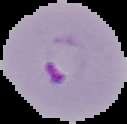
result: malaria parasites identified
image_type: cell region segmented out of the field of view; surrounding area masked to black
image_size: 127×124 pixels
preparation: thin blood film